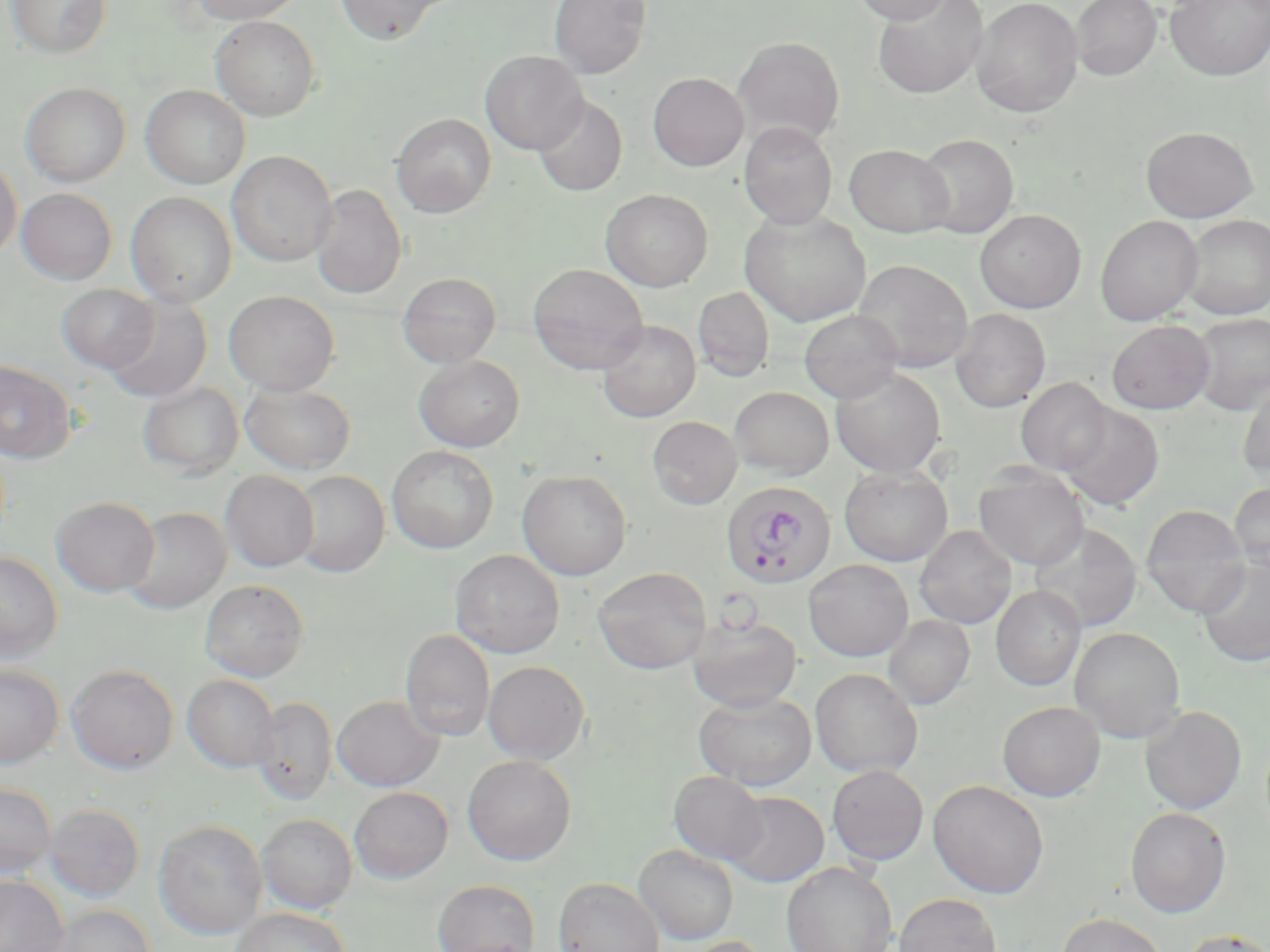 Approximate bounding boxes as (x1, y1, x2, y2) in pixels. Plasmodium falciparum-infected red blood cell locations: (721, 480, 836, 589). Uninfected red blood cell locations: (5, 0, 113, 59), (190, 0, 308, 24), (334, 0, 442, 45), (549, 0, 652, 78), (851, 0, 953, 25), (971, 0, 1083, 118), (1072, 0, 1162, 81), (1164, 0, 1270, 81), (873, 1, 989, 99), (210, 15, 321, 121), (732, 36, 845, 146), (480, 50, 587, 154), (648, 72, 749, 172), (20, 82, 131, 187), (140, 85, 251, 189), (533, 95, 628, 196), (391, 113, 496, 218), (739, 122, 838, 229), (1141, 126, 1258, 223), (917, 133, 1018, 238), (845, 144, 954, 238), (226, 151, 337, 267), (0, 155, 22, 261), (311, 183, 407, 300), (16, 188, 118, 284), (601, 189, 713, 291), (126, 192, 237, 307), (739, 209, 871, 327), (975, 209, 1086, 313), (1095, 215, 1203, 325), (1182, 215, 1270, 320), (853, 259, 973, 373), (528, 264, 649, 374), (397, 272, 501, 369), (56, 284, 159, 373), (693, 286, 774, 382), (223, 290, 340, 395), (103, 296, 212, 403), (950, 308, 1051, 412), (799, 310, 903, 403), (1190, 313, 1270, 414), (597, 320, 700, 422), (1107, 320, 1215, 414), (414, 355, 525, 452), (0, 359, 77, 464), (830, 367, 946, 477), (1015, 377, 1113, 477), (1238, 377, 1270, 478), (138, 382, 244, 479), (240, 382, 356, 475), (729, 386, 834, 480), (1055, 401, 1165, 511), (647, 416, 742, 510), (386, 445, 498, 554), (839, 465, 953, 566), (974, 465, 1089, 570), (517, 469, 632, 580), (220, 470, 319, 572), (289, 470, 390, 577), (1229, 481, 1270, 576), (52, 496, 160, 597), (1141, 504, 1250, 617), (120, 506, 231, 614), (1030, 524, 1143, 633), (914, 525, 1016, 628), (450, 549, 565, 658), (0, 550, 63, 662), (1196, 557, 1270, 668), (803, 559, 913, 661), (593, 566, 712, 674), (200, 579, 309, 682), (990, 585, 1087, 691), (687, 614, 803, 712), (884, 615, 975, 709), (1069, 627, 1186, 742), (400, 628, 495, 741), (483, 660, 589, 764), (0, 663, 64, 768), (67, 664, 179, 773), (810, 668, 923, 778), (182, 674, 280, 772), (693, 691, 816, 789), (332, 695, 444, 792), (251, 696, 337, 805), (997, 701, 1105, 801), (1140, 705, 1246, 814), (462, 755, 577, 865), (827, 765, 928, 865), (669, 771, 767, 865), (928, 779, 1049, 898), (0, 781, 57, 879), (349, 786, 453, 884), (724, 791, 828, 887), (44, 803, 145, 902), (1125, 806, 1231, 917), (257, 813, 357, 913), (154, 819, 268, 939), (633, 844, 739, 944), (781, 861, 897, 952), (1, 875, 68, 952), (554, 877, 664, 952), (432, 879, 540, 952), (894, 893, 1003, 952), (48, 903, 156, 952), (230, 906, 351, 952), (1057, 912, 1167, 952), (1176, 929, 1270, 952), (671, 936, 773, 952). Slide-level diagnosis: Plasmodium falciparum. Light microscopy. May-Grünwald-Giemsa stain. Image is 1270×952 pixels. 1000x magnification. Single field of view. Thin blood film.